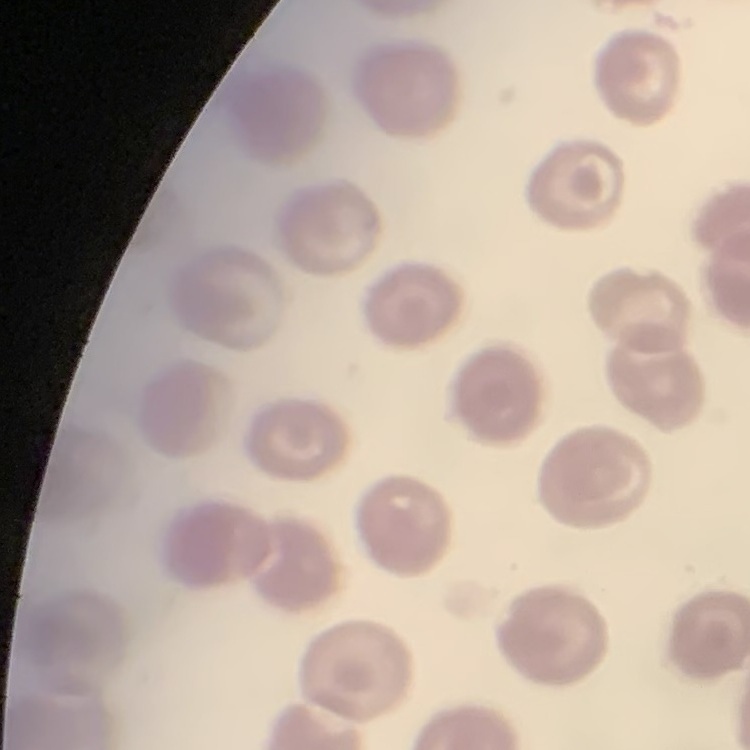
The red blood cells exhibit no rouleaux formation. Field's or Giemsa stain. Square crop of a larger photomicrograph. Thin blood film.